Give the position of every Plasmodium parasite.
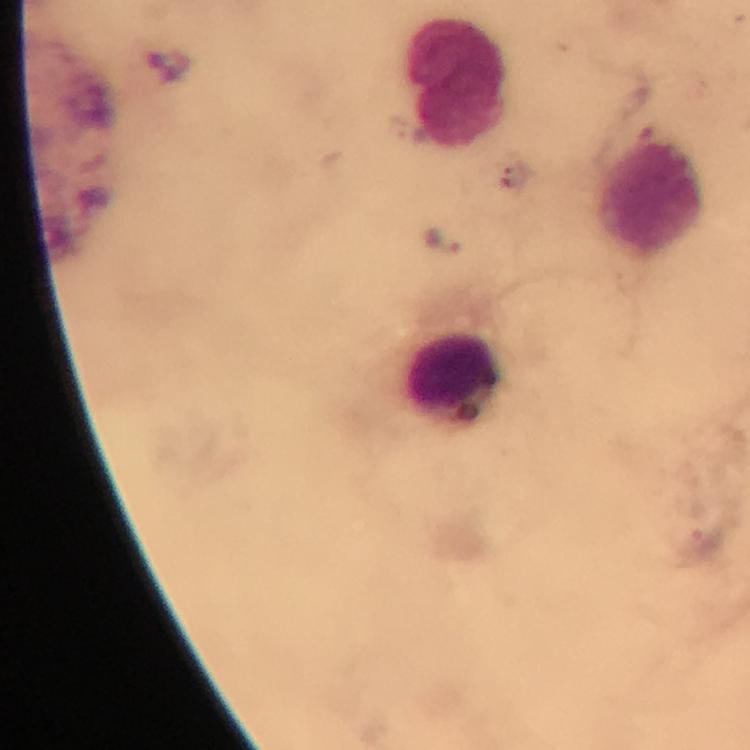
Approximate centers as (x, y) in pixels.
Plasmodium parasites: (444, 243).

cropped from = one field of view
immersion oil = applied
stain = Giemsa
magnification = 100x
preparation = thick blood film
leukocyte locations = approximate centers as (x, y) in pixels: (462, 81), (646, 195), (455, 376)
image size = 750×750 pixels
context = from a malaria diagnostic workup
capture = smartphone mounted on the microscope